State which parasite is depicted.
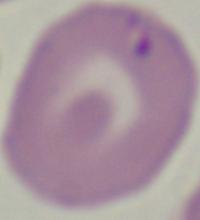
This is Babesia.

1000x magnification. Micrograph.